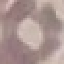
Result: negative for malaria parasites. Thin blood film. Giemsa stain. Acquired by smartphone through the microscope eyepiece. Automatically extracted cell patch, resized to 64 × 64 pixels.